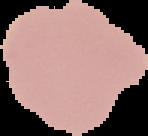

Summary:
  - Result: negative for Plasmodium parasites
  - Image type: segmented cell region with the area outside set to black
  - Image size: 148×136 pixels
  - Preparation: thin blood smear